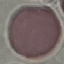
result = no malaria parasites seen
capture = smartphone camera at the microscope eyepiece
image type = automatically extracted cell patch, resized to 64 × 64 pixels
stain = Giemsa
preparation = thin smear